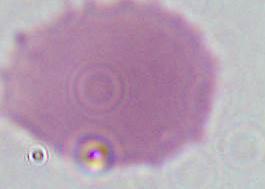

Summary:
  - Modality: photomicrograph
  - Magnification: 1000x
  - Identification: erythrocyte